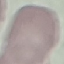
malaria status = uninfected
stain = Giemsa
preparation = thin smear
image type = automatically extracted cell patch, resized to 64 × 64 pixels
capture = smartphone camera at the microscope eyepiece